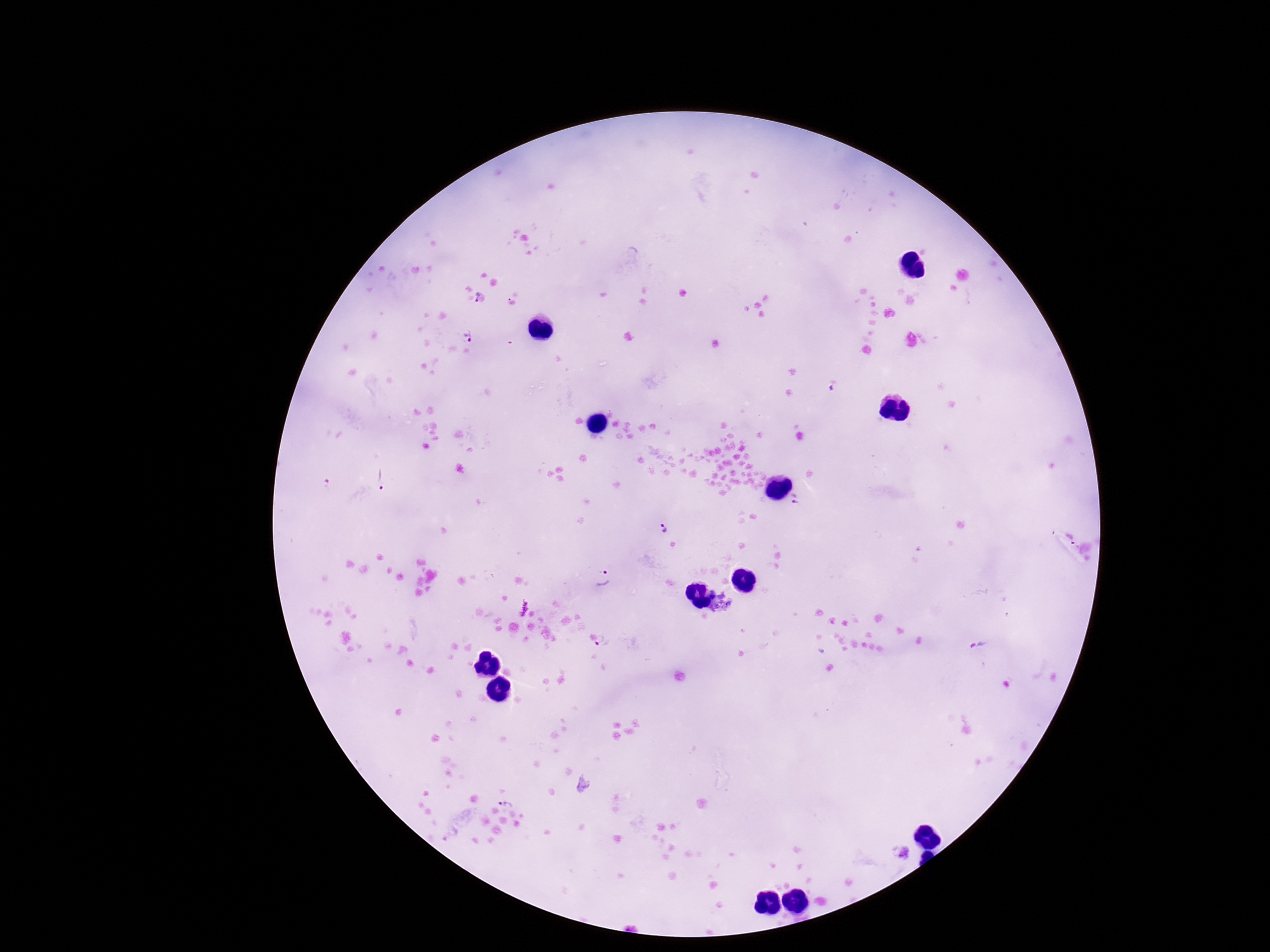
Approximate centers as {x, y} in pixels.
Summary:
  - Plasmodium parasite locations: {478, 296}, {511, 303}, {468, 337}, {380, 480}, {796, 499}, {663, 529}, {602, 578}, {602, 644}, {507, 799}, {905, 853}
  - Stain: Giemsa
  - Preparation: thick peripheral-blood smear
  - Magnification: 100x
  - Capture: smartphone camera through the microscope eyepiece
  - Patient malaria status: positive
  - Field of view: one from this slide
  - Image size: 1270×952 pixels